State the blood parasite species.
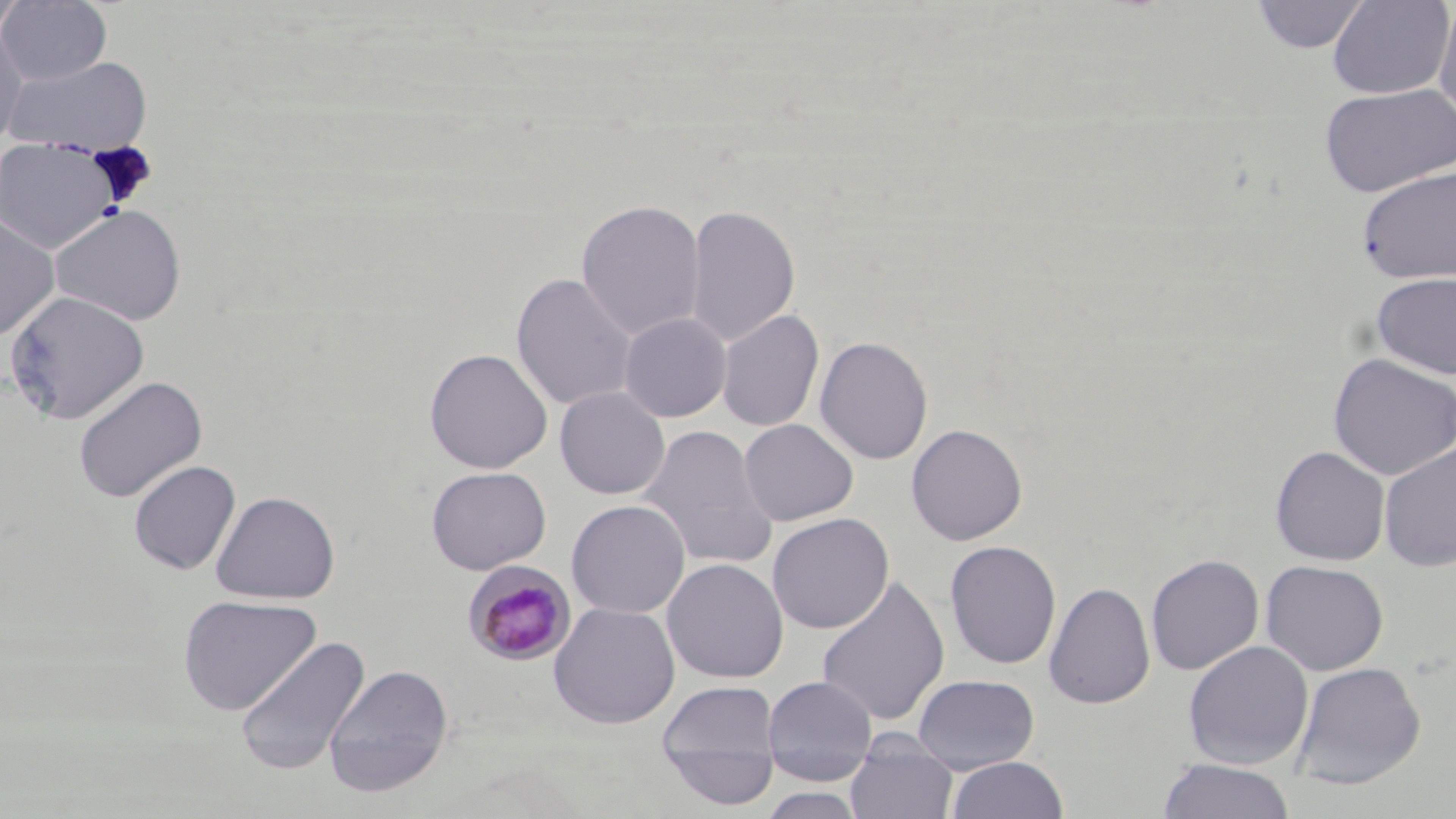

Plasmodium malariae.

Approximate bounding boxes as (x1,y1)-(x2,y2) corner pairs in pixels. Plasmodium malariae-infected red blood cell locations: (463,561)-(577,666). Uninfected red blood cell locations: (0,0)-(112,86), (0,0)-(30,43), (1251,0)-(1371,55), (1327,0)-(1455,99), (1434,3)-(1456,124), (0,20)-(29,151), (2,54)-(154,156), (1319,82)-(1456,197), (0,138)-(123,256), (1356,164)-(1456,285), (576,199)-(705,340), (50,204)-(186,325), (685,204)-(800,347), (0,211)-(60,342), (1370,271)-(1456,380), (511,272)-(637,411), (3,291)-(151,425), (716,309)-(824,432), (619,312)-(732,422), (814,336)-(933,465), (424,348)-(553,474), (1327,353)-(1455,479), (433,366)-(665,482), (73,375)-(207,503), (554,387)-(670,500), (739,419)-(858,526), (905,423)-(1027,546), (637,424)-(779,570), (1378,442)-(1456,572), (1270,445)-(1390,566), (128,460)-(241,575), (426,466)-(551,574), (210,490)-(340,604), (566,499)-(691,619), (767,513)-(893,633), (944,540)-(1062,670), (1145,553)-(1264,676), (661,558)-(788,684), (1260,559)-(1389,675), (815,574)-(950,727), (1043,582)-(1155,709), (178,595)-(321,715), (548,601)-(681,729), (234,633)-(370,777), (1183,641)-(1314,771), (1291,661)-(1426,790), (324,663)-(454,799), (912,673)-(1040,773), (762,675)-(878,786), (655,681)-(781,801), (1165,683)-(1309,814), (846,734)-(958,819), (946,756)-(1069,819), (1156,758)-(1295,818), (758,788)-(868,818). Image is 1456×819 pixels. Optical microscopy. Thin blood smear. One field of a larger specimen. May-Grünwald-Giemsa-stained preparation. 1000x magnification.